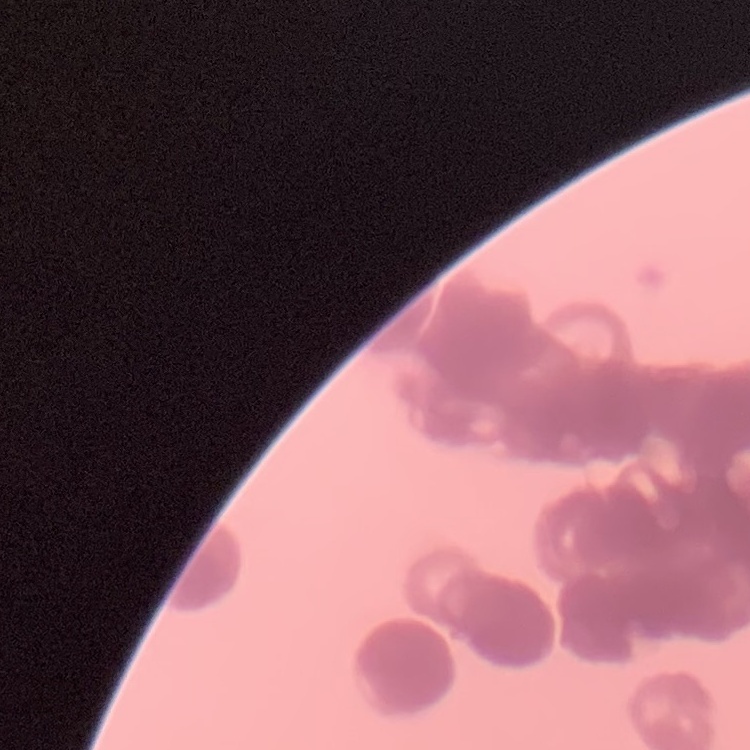 The red blood cells show rouleaux formation. Field's or Giemsa stain. Thin blood film. Square crop of a larger photomicrograph.